Identify the blood parasite species.
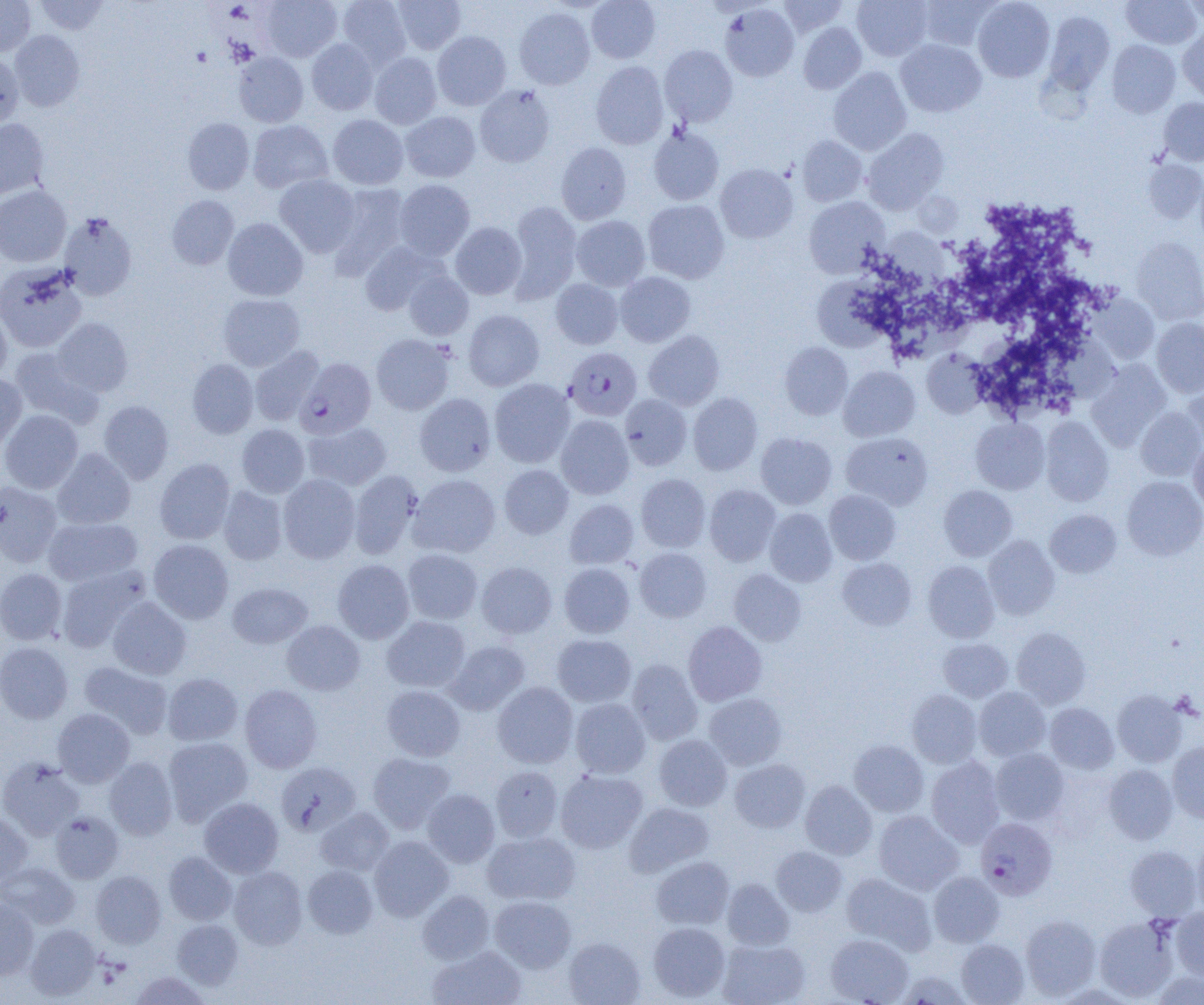
Plasmodium falciparum.

Summary:
  - Coordinate format: approximate bounding boxes as (x1, y1, x2, y2) in pixels
  - Uninfected red blood cell locations: (0, 0, 36, 56), (35, 0, 110, 35), (261, 0, 342, 61), (338, 0, 411, 67), (392, 0, 466, 54), (586, 0, 660, 63), (777, 0, 850, 36), (852, 0, 933, 61), (916, 0, 997, 51), (973, 0, 1055, 82), (1121, 0, 1202, 49), (1183, 0, 1204, 27), (720, 3, 800, 82), (515, 7, 595, 89), (1044, 11, 1115, 94), (798, 22, 867, 94), (1178, 29, 1204, 101), (10, 30, 85, 112), (432, 31, 511, 110), (307, 39, 378, 115), (896, 39, 986, 117), (1107, 40, 1180, 117), (660, 45, 738, 127), (0, 52, 23, 130), (234, 52, 308, 127), (369, 53, 442, 128), (590, 61, 669, 149), (829, 67, 911, 155), (475, 84, 556, 167), (1159, 97, 1204, 165), (401, 111, 480, 182), (328, 114, 408, 189), (0, 118, 49, 200), (182, 118, 254, 194), (248, 120, 332, 193), (648, 127, 725, 205), (863, 128, 948, 214), (797, 135, 867, 206), (556, 142, 632, 224), (1143, 160, 1204, 223), (715, 163, 798, 243), (1195, 170, 1204, 250), (274, 174, 360, 256), (394, 179, 475, 260), (329, 182, 410, 274), (0, 185, 71, 267), (167, 195, 240, 270), (805, 196, 889, 278), (643, 200, 729, 283), (507, 201, 582, 302), (58, 212, 137, 300), (572, 215, 650, 291), (222, 218, 308, 301), (450, 222, 527, 299), (883, 228, 944, 283), (1132, 237, 1204, 324), (359, 241, 446, 316), (0, 262, 87, 353), (404, 271, 474, 340), (615, 272, 696, 347), (814, 274, 895, 349), (551, 279, 623, 349), (218, 293, 305, 370), (1090, 294, 1160, 363), (0, 307, 11, 385), (463, 310, 544, 390), (52, 318, 133, 396), (1152, 318, 1204, 397), (644, 330, 724, 410), (371, 334, 454, 415), (779, 342, 853, 420), (249, 346, 324, 425), (10, 347, 102, 427), (922, 349, 989, 418), (187, 359, 258, 438), (1086, 360, 1171, 450), (838, 366, 920, 441), (1183, 373, 1204, 451), (0, 374, 27, 451), (490, 378, 575, 468), (414, 393, 496, 476), (688, 393, 763, 475), (620, 394, 692, 471), (99, 400, 174, 483), (1136, 407, 1204, 480), (0, 409, 83, 494), (556, 415, 634, 499), (1040, 417, 1113, 506), (971, 418, 1050, 494), (303, 420, 391, 490), (236, 424, 309, 497), (841, 432, 933, 510), (755, 433, 836, 509), (1189, 441, 1204, 513), (53, 448, 136, 529), (154, 458, 235, 544), (499, 465, 573, 539), (349, 470, 423, 558), (278, 474, 360, 563), (409, 474, 500, 557), (636, 474, 711, 552), (1122, 476, 1204, 560), (0, 481, 62, 567), (704, 484, 781, 565), (218, 485, 288, 565), (938, 485, 1017, 561), (824, 489, 901, 565), (565, 499, 639, 569), (764, 508, 837, 586), (1045, 509, 1121, 578), (43, 517, 142, 586), (983, 535, 1059, 620), (148, 539, 234, 623), (635, 547, 711, 622), (403, 549, 482, 624), (837, 557, 917, 630), (333, 559, 414, 643), (923, 561, 1000, 642), (476, 562, 557, 639), (559, 562, 635, 638), (57, 566, 149, 652), (0, 568, 67, 644), (728, 569, 807, 646), (227, 582, 312, 648), (107, 597, 191, 679), (382, 616, 470, 692), (282, 620, 365, 695), (683, 621, 766, 706), (1012, 627, 1091, 708), (552, 634, 636, 706), (938, 638, 1013, 702), (445, 640, 530, 715), (0, 642, 73, 724), (626, 659, 702, 745), (79, 661, 172, 739), (163, 672, 243, 745), (492, 682, 577, 768), (240, 684, 322, 773), (381, 685, 465, 761), (974, 687, 1050, 761), (906, 689, 982, 768), (1112, 690, 1187, 767), (704, 693, 787, 770), (570, 698, 651, 778), (1045, 702, 1119, 774), (54, 708, 135, 786), (654, 734, 732, 811), (164, 736, 253, 824), (849, 740, 928, 817), (1167, 742, 1204, 822), (990, 748, 1070, 825), (367, 752, 455, 833), (0, 757, 84, 840), (104, 757, 177, 840), (926, 757, 1005, 848), (729, 759, 810, 832), (276, 761, 361, 836), (1103, 764, 1178, 844), (491, 765, 562, 842), (556, 769, 648, 853), (800, 780, 877, 859), (423, 789, 500, 867), (199, 797, 283, 877), (624, 802, 714, 877), (315, 808, 394, 876), (873, 810, 963, 894), (50, 811, 123, 883), (0, 812, 33, 886), (482, 831, 579, 905), (369, 835, 454, 921), (1192, 837, 1204, 918), (1124, 844, 1202, 920), (771, 846, 847, 917), (164, 852, 237, 925), (651, 856, 734, 930), (0, 862, 80, 928), (303, 865, 378, 938), (229, 866, 307, 949), (91, 870, 166, 948), (841, 872, 936, 954), (928, 872, 1005, 947), (722, 878, 794, 951), (417, 890, 494, 964), (489, 896, 576, 973), (0, 899, 39, 979), (1170, 907, 1204, 980), (1020, 914, 1102, 999), (1094, 915, 1179, 1002), (172, 919, 244, 990), (648, 922, 730, 1001), (26, 924, 101, 1000), (825, 933, 913, 1005), (563, 937, 645, 1005), (717, 939, 810, 1005), (956, 939, 1029, 1005), (428, 946, 526, 1005), (897, 970, 972, 1005), (131, 971, 210, 1004), (1152, 971, 1204, 1005)
  - Plasmodium falciparum-infected red blood cell locations: (567, 351, 646, 425), (295, 357, 376, 439), (975, 817, 1057, 899)
  - Field of view: single
  - Magnification: 1000x
  - Image size: 1204×1005 pixels
  - Preparation: thin blood film
  - Modality: optical microscopy